Assess this cell for malaria.
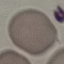
Uninfected.

Summary:
  - Preparation: thin blood smear
  - Capture: smartphone camera at the microscope eyepiece
  - Stain: Giemsa
  - Image type: cell patch, automatically extracted from a larger field of view and resized to 64 × 64 pixels